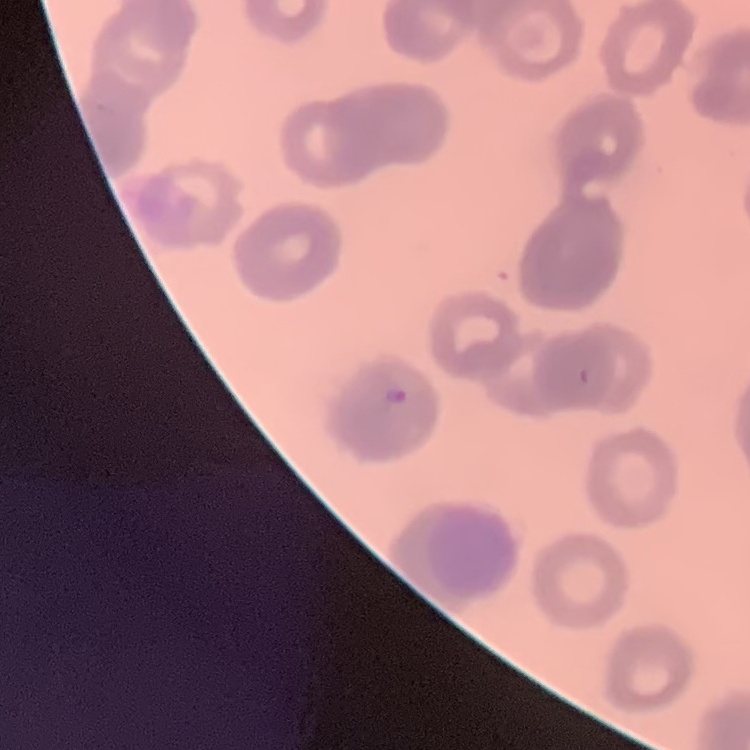
The red blood cells show rouleaux formation. Stained with either Field's or Giemsa. Thin blood smear. Square crop of a larger photomicrograph.